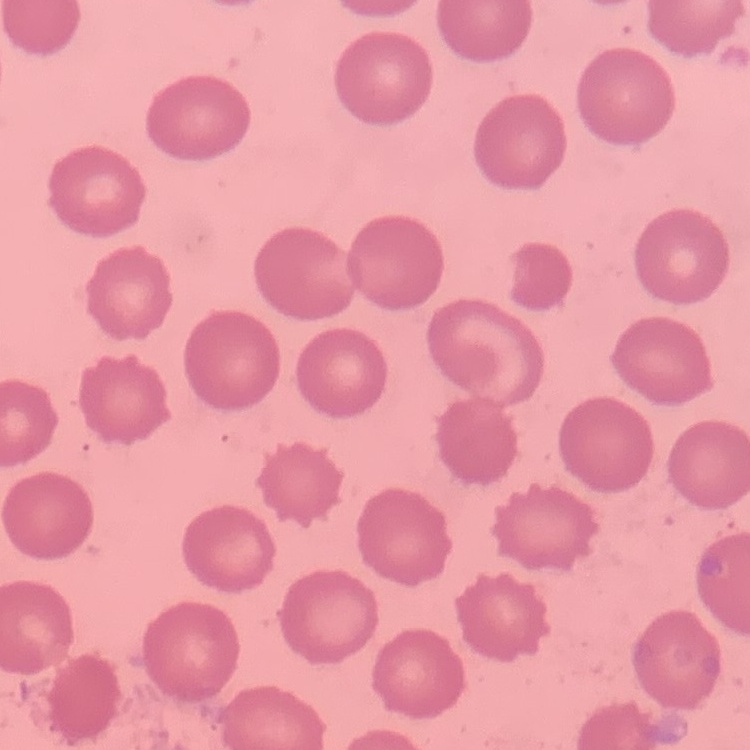
{
  "red_blood_cell_morphology": "no rouleaux formation",
  "image_type": "one tile cut from a larger photomicrograph",
  "preparation": "thin peripheral smear",
  "stain": "Field's or Giemsa"
}